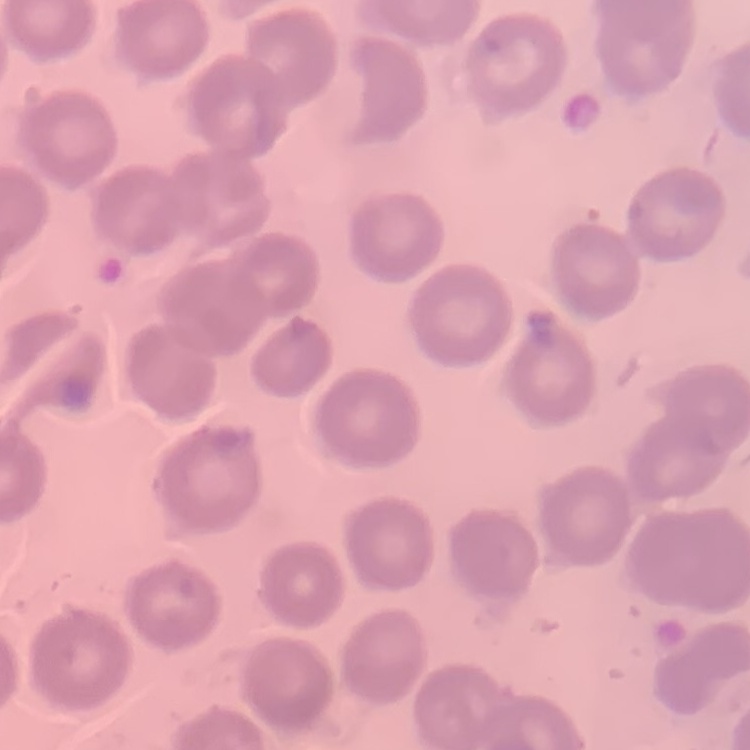
The erythrocytes exhibit no rouleaux formation. Thin peripheral smear. Field's or Giemsa stain. One tile cut from a larger photomicrograph.